Assess this cell for malaria.
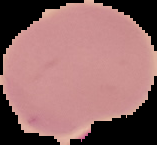

Uninfected.

image type = segmented cell region on a black background
preparation = thin blood film
image size = 157×145 pixels